Comment on the morphology of the red blood cells.
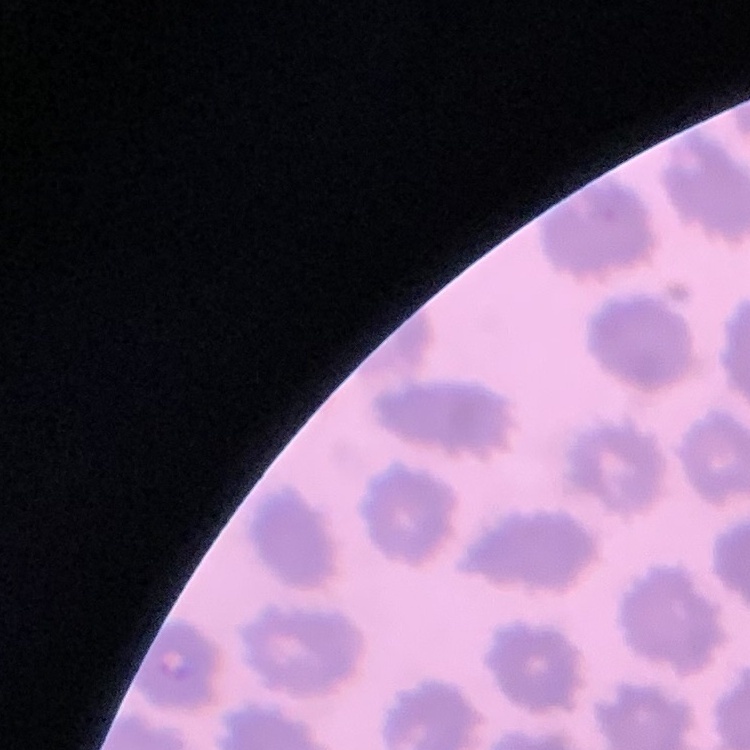
They show no rouleaux formation.

stain = Field's or Giemsa
image type = one tile cut from a larger photomicrograph
preparation = thin peripheral smear